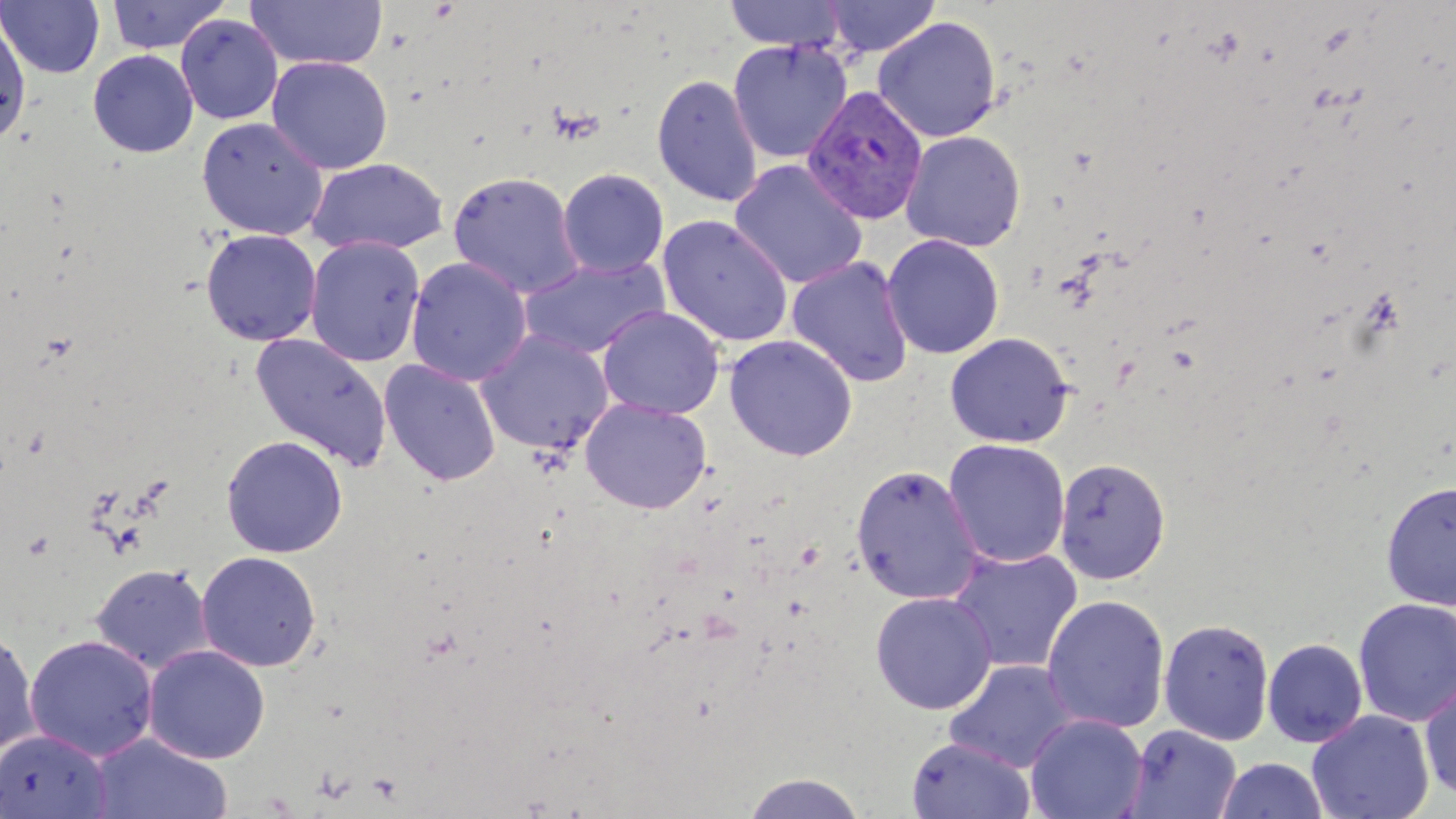

Approximate bounding boxes as (x1,y1)-(x2,y2) corner pairs in pixels. Plasmodium vivax-infected red blood cell locations: (802,85)-(929,225). Uninfected red blood cell locations: (107,0)-(230,54), (245,0)-(388,70), (822,0)-(941,58), (1,1)-(105,78), (721,1)-(847,51), (0,13)-(31,145), (176,14)-(283,124), (873,16)-(1002,142), (727,40)-(852,163), (88,50)-(198,158), (268,56)-(393,174), (652,73)-(763,208), (197,116)-(328,239), (900,130)-(1026,252), (306,157)-(450,256), (728,159)-(868,289), (557,168)-(669,279), (448,170)-(585,299), (657,214)-(794,348), (200,228)-(322,347), (882,234)-(1005,360), (305,237)-(426,367), (785,255)-(915,389), (406,257)-(532,387), (518,257)-(669,360), (597,305)-(724,420), (475,330)-(613,456), (249,332)-(393,471), (945,332)-(1074,449), (724,334)-(858,462), (378,359)-(502,486), (580,397)-(712,514), (221,435)-(348,558), (943,438)-(1071,568), (1054,457)-(1171,584), (850,463)-(984,605), (1380,480)-(1456,610), (946,547)-(1083,675), (196,551)-(322,672), (90,563)-(214,674), (869,591)-(997,715), (79,593)-(238,754), (1041,594)-(1170,734), (1352,597)-(1456,728), (1158,618)-(1274,745), (0,626)-(40,758), (24,635)-(159,761), (1262,638)-(1368,747), (143,644)-(271,764), (944,659)-(1079,773), (1419,674)-(1456,803), (1307,710)-(1434,819), (1024,714)-(1149,819), (1121,723)-(1242,819), (0,729)-(112,819), (91,734)-(232,819), (907,737)-(1036,818), (1215,757)-(1329,819), (741,772)-(869,818). Slide-level diagnosis: Plasmodium vivax. Single field of view. Image is 1456×819 pixels. Thin blood smear. May-Grünwald-Giemsa stain. 1000x magnification. Optical microscopy.